Give the position of every Plasmodium parasite.
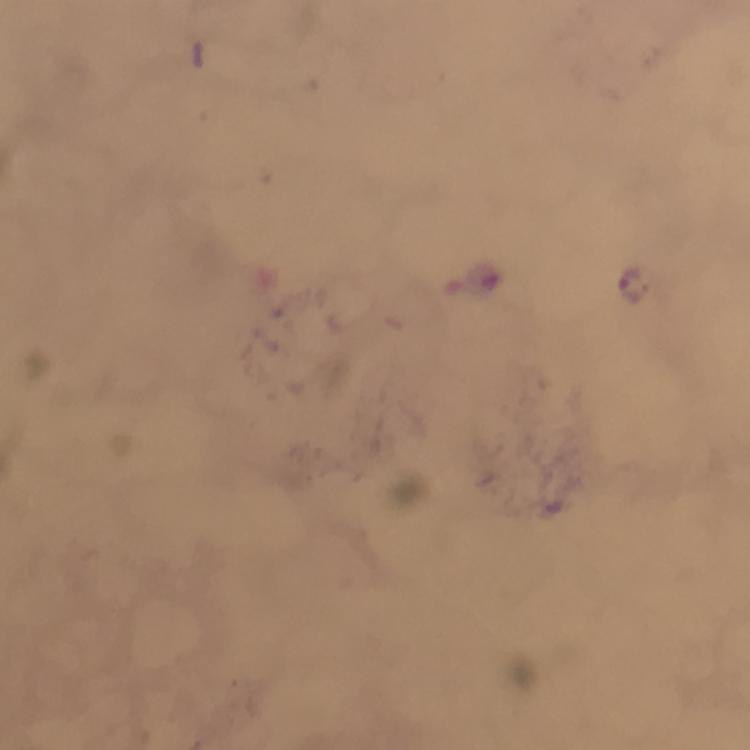
Approximate centers as {x, y} in pixels.
Plasmodium parasites: {632, 285}.

{
  "context": "from a malaria diagnostic workup",
  "immersion_oil": "used",
  "magnification": "100x",
  "stain": "Giemsa",
  "preparation": "thick smear",
  "cropped_from": "a single field of view",
  "image_size": "750×750 pixels",
  "capture": "smartphone camera through the microscope"
}